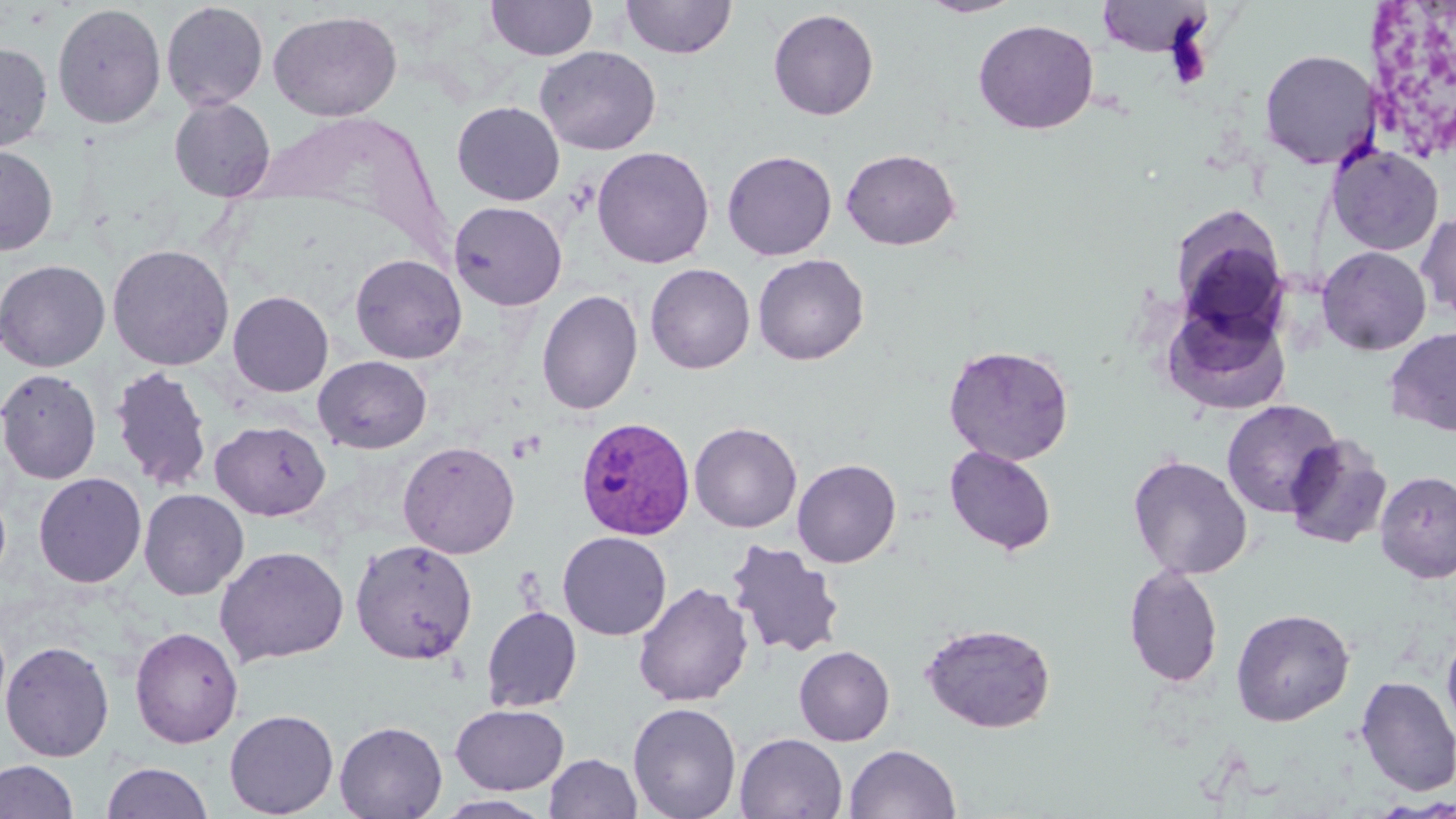
Approximate bounding boxes as (x1, y1, x2, y2) in pixels. Platelet locations: (509, 431, 545, 461). Uninfected red blood cell locations: (486, 0, 598, 61), (917, 0, 1026, 18), (1096, 0, 1212, 57), (620, 1, 737, 60), (161, 2, 269, 111), (52, 3, 166, 130), (768, 8, 879, 121), (268, 10, 402, 121), (973, 19, 1099, 135), (0, 42, 53, 155), (535, 45, 661, 155), (1259, 48, 1380, 170), (169, 97, 276, 202), (451, 101, 565, 205), (1326, 143, 1444, 256), (0, 144, 58, 255), (592, 146, 714, 268), (840, 148, 961, 250), (722, 150, 837, 261), (448, 201, 567, 311), (1169, 205, 1291, 336), (1416, 211, 1456, 323), (107, 243, 234, 371), (1317, 246, 1431, 355), (350, 253, 467, 364), (752, 253, 870, 365), (0, 259, 111, 371), (645, 263, 755, 374), (228, 290, 333, 397), (536, 290, 642, 415), (1163, 299, 1291, 414), (1384, 327, 1456, 436), (943, 344, 1074, 466), (313, 355, 432, 454), (109, 365, 213, 493), (0, 368, 102, 484), (1221, 399, 1342, 518), (210, 420, 331, 521), (689, 422, 802, 533), (1283, 433, 1392, 550), (397, 440, 520, 559), (944, 445, 1057, 556), (1128, 455, 1253, 579), (792, 458, 901, 568), (1374, 470, 1456, 583), (33, 472, 147, 588), (138, 488, 249, 600), (557, 531, 672, 640), (350, 539, 478, 665), (725, 539, 846, 659), (215, 545, 349, 666), (1123, 564, 1224, 688), (633, 582, 754, 707), (481, 605, 582, 713), (1231, 607, 1355, 726), (919, 622, 1057, 734), (129, 625, 244, 748), (1442, 631, 1456, 744), (0, 640, 115, 762), (794, 645, 895, 746), (1355, 676, 1456, 796), (627, 702, 743, 819), (449, 703, 570, 795), (224, 708, 339, 818), (334, 720, 447, 818), (734, 733, 848, 818), (844, 744, 961, 819), (544, 753, 642, 818), (0, 760, 79, 819), (102, 761, 213, 819), (432, 794, 555, 818). Plasmodium vivax-infected red blood cell locations: (574, 415, 696, 540). Slide-level diagnosis: Plasmodium vivax. Image is 1456×819 pixels. Single field of view. Thin blood smear. Captured at 1000x magnification. Light microscopy. May-Grünwald-Giemsa stain.